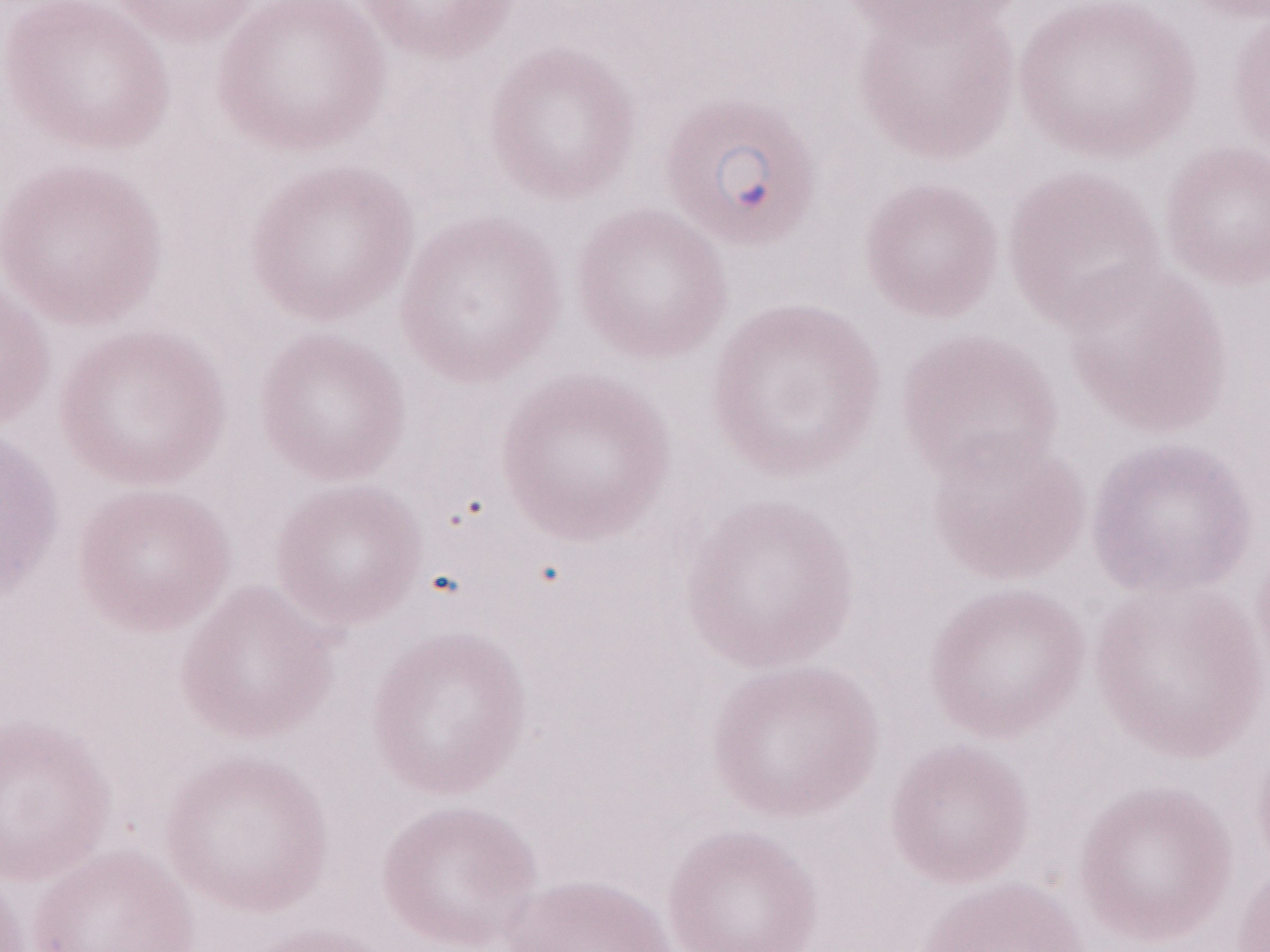
Image is 1270×952 pixels. Patient diagnosis: malaria infection. Magnification: 1,000x. May-Grünwald-Giemsa-stained preparation. Olympus BX43 microscope, Olympus DP73 camera. Single field of view. Thin blood smear.